State which parasite is depicted.
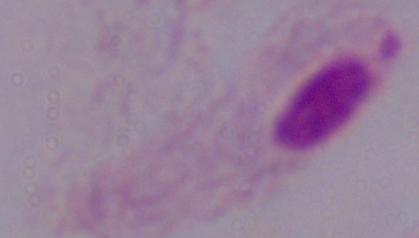

A trichomonad.

Summary:
  - Magnification: 1000x
  - Modality: photomicrograph